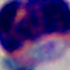

{
  "modality": "micrograph",
  "identification": "white blood cell",
  "magnification": "1000x"
}